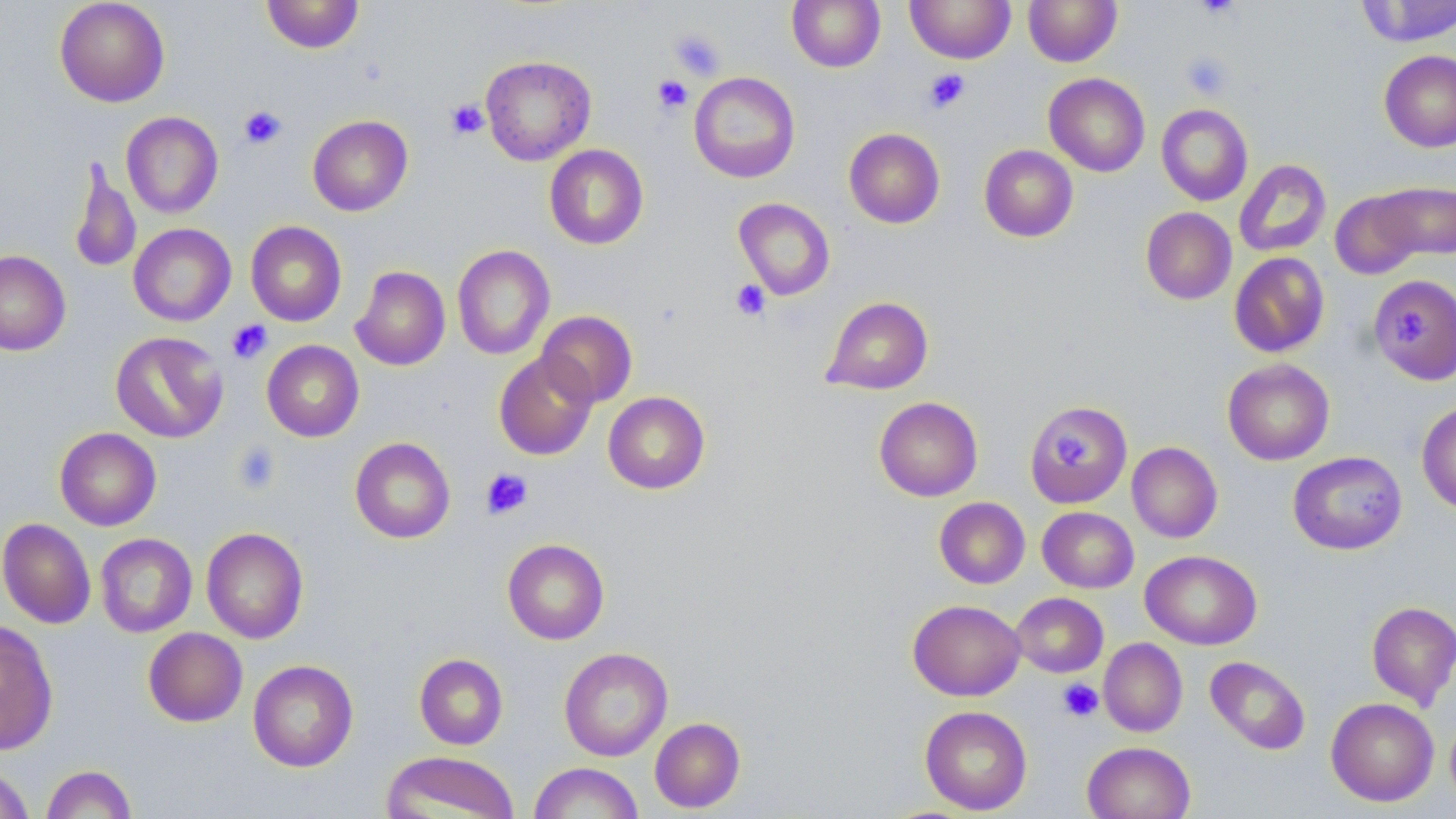

Approximate bounding boxes as named x1/y1/x2/y2 corners in pixels. Uninfected red blood cell locations: (x1=54, y1=0, x2=170, y2=107), (x1=261, y1=0, x2=365, y2=53), (x1=787, y1=0, x2=886, y2=72), (x1=905, y1=0, x2=1015, y2=64), (x1=1023, y1=0, x2=1122, y2=67), (x1=1355, y1=1, x2=1455, y2=47), (x1=1379, y1=50, x2=1456, y2=152), (x1=480, y1=55, x2=596, y2=165), (x1=689, y1=72, x2=800, y2=183), (x1=1044, y1=73, x2=1150, y2=177), (x1=1156, y1=103, x2=1253, y2=206), (x1=121, y1=112, x2=223, y2=218), (x1=307, y1=115, x2=413, y2=216), (x1=843, y1=127, x2=945, y2=228), (x1=544, y1=144, x2=649, y2=250), (x1=979, y1=145, x2=1078, y2=242), (x1=68, y1=159, x2=141, y2=275), (x1=1234, y1=159, x2=1331, y2=257), (x1=1373, y1=180, x2=1456, y2=261), (x1=1330, y1=189, x2=1425, y2=280), (x1=733, y1=198, x2=835, y2=301), (x1=1140, y1=207, x2=1236, y2=305), (x1=245, y1=221, x2=347, y2=326), (x1=128, y1=223, x2=236, y2=326), (x1=452, y1=244, x2=555, y2=360), (x1=0, y1=250, x2=71, y2=355), (x1=1229, y1=252, x2=1330, y2=358), (x1=350, y1=266, x2=450, y2=371), (x1=1368, y1=274, x2=1456, y2=384), (x1=820, y1=295, x2=934, y2=396), (x1=536, y1=310, x2=638, y2=407), (x1=110, y1=331, x2=228, y2=443), (x1=262, y1=340, x2=364, y2=442), (x1=493, y1=351, x2=599, y2=460), (x1=1222, y1=359, x2=1334, y2=465), (x1=602, y1=391, x2=710, y2=494), (x1=874, y1=397, x2=983, y2=501), (x1=1027, y1=399, x2=1135, y2=508), (x1=1416, y1=401, x2=1456, y2=515), (x1=54, y1=427, x2=161, y2=530), (x1=350, y1=437, x2=456, y2=544), (x1=1127, y1=442, x2=1222, y2=543), (x1=1288, y1=451, x2=1408, y2=555), (x1=934, y1=497, x2=1030, y2=589), (x1=1037, y1=506, x2=1139, y2=593), (x1=0, y1=518, x2=96, y2=629), (x1=201, y1=527, x2=309, y2=643), (x1=95, y1=533, x2=197, y2=637), (x1=502, y1=538, x2=610, y2=645), (x1=1140, y1=549, x2=1262, y2=650), (x1=1011, y1=592, x2=1108, y2=678), (x1=908, y1=599, x2=1026, y2=701), (x1=1366, y1=601, x2=1456, y2=710), (x1=0, y1=620, x2=58, y2=755), (x1=143, y1=627, x2=248, y2=727), (x1=1099, y1=637, x2=1188, y2=737), (x1=559, y1=647, x2=673, y2=761), (x1=414, y1=653, x2=508, y2=750), (x1=1205, y1=656, x2=1311, y2=755), (x1=247, y1=660, x2=358, y2=772), (x1=1325, y1=697, x2=1439, y2=806), (x1=919, y1=706, x2=1032, y2=815), (x1=650, y1=717, x2=745, y2=813), (x1=1082, y1=741, x2=1195, y2=819), (x1=382, y1=751, x2=521, y2=819), (x1=529, y1=762, x2=644, y2=818), (x1=0, y1=764, x2=34, y2=819), (x1=41, y1=764, x2=137, y2=819). Platelet locations: (x1=1195, y1=0, x2=1241, y2=21), (x1=668, y1=27, x2=726, y2=80), (x1=1180, y1=51, x2=1234, y2=101), (x1=923, y1=69, x2=970, y2=113), (x1=652, y1=75, x2=693, y2=115), (x1=445, y1=98, x2=489, y2=140), (x1=239, y1=105, x2=287, y2=149), (x1=730, y1=279, x2=770, y2=322), (x1=1396, y1=308, x2=1429, y2=349), (x1=227, y1=319, x2=273, y2=364), (x1=1048, y1=432, x2=1086, y2=466), (x1=232, y1=441, x2=282, y2=494), (x1=480, y1=468, x2=532, y2=519), (x1=1057, y1=678, x2=1103, y2=722). Slide-level diagnosis: no evidence of blood parasites. Captured at 1000x magnification. May-Grünwald-Giemsa-stained preparation. Image is 1456×819 pixels. Single field of view. Light microscopy. Thin blood film.